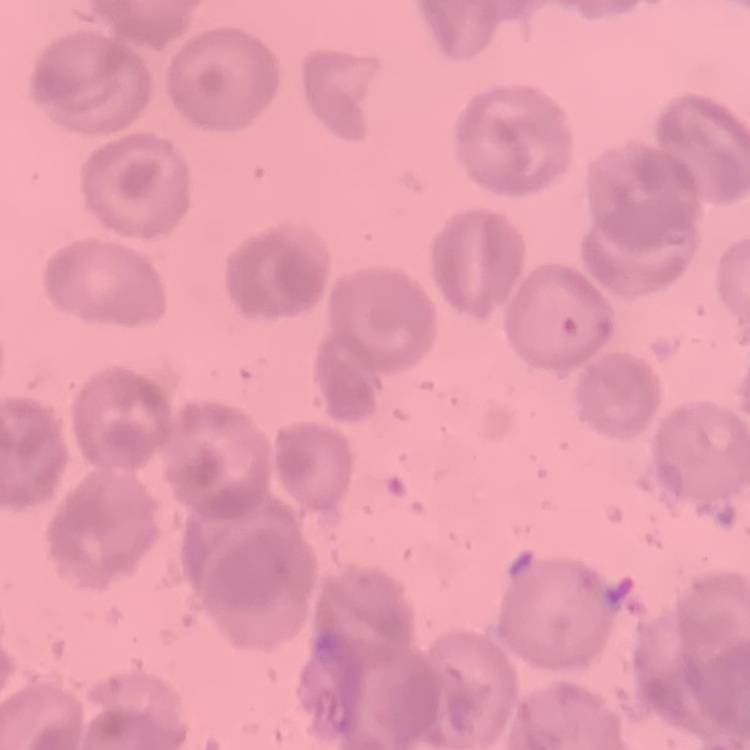

Summary:
  - Erythrocyte morphology: no rouleaux formation
  - Preparation: thin peripheral smear
  - Image type: one tile cut from a larger photomicrograph
  - Stain: Field's or Giemsa